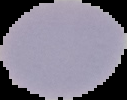
Summary:
  - Result: negative for malaria parasites
  - Image type: segmented cell region on a black background
  - Image size: 127×100 pixels
  - Preparation: thin blood film